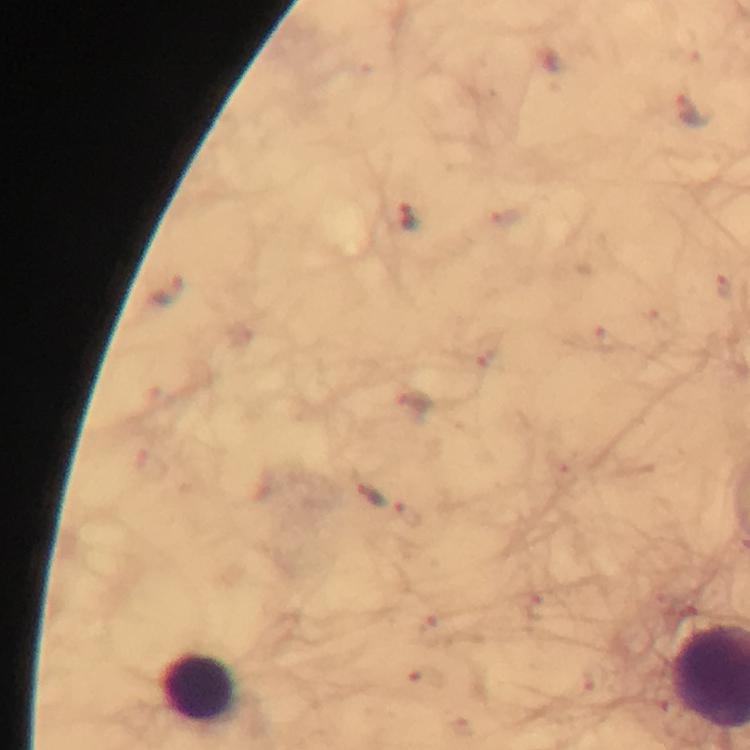

Approximate centers as [x, y] in pixels. Leukocyte locations: [198, 689]. Malaria parasite locations: [694, 108], [506, 215], [408, 217], [725, 288], [164, 291], [605, 339], [484, 350], [413, 404], [368, 494], [406, 515], [537, 606], [430, 630], [423, 678]. Thick blood film. Cropped region of a single field of view. Image is 750×750 pixels. 100x magnification. Immersion oil applied. Giemsa-stained preparation. From a diagnostic examination for malaria. Photographed through the microscope with a smartphone camera.